Name the parasite shown.
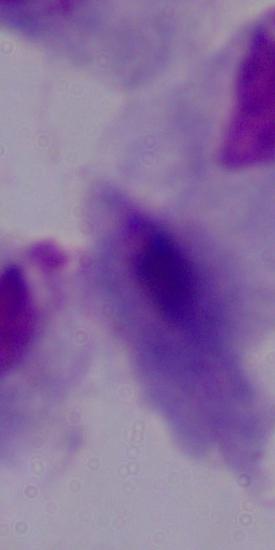
This is a trichomonad.

magnification = 1000x
modality = photomicrograph